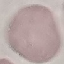

{
  "malaria_status": "uninfected",
  "capture": "smartphone through the microscope eyepiece",
  "image_type": "cell patch, automatically extracted from a larger field of view and resized to 64 × 64 pixels",
  "preparation": "thin smear",
  "stain": "Giemsa"
}